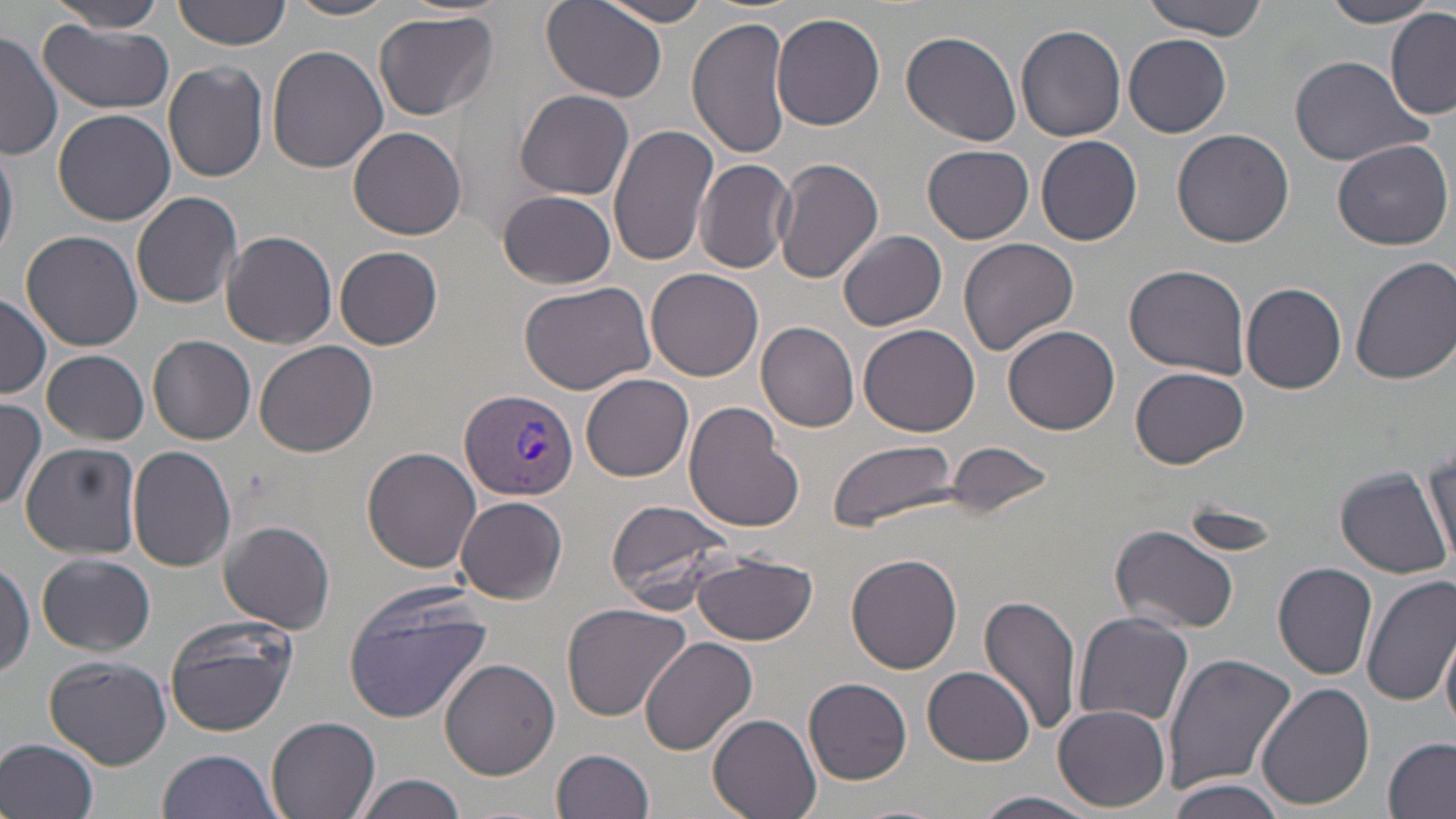 Approximate bounding boxes as [x1, y1, x2, y2] in pixels. Uninfected red blood cell locations: [44, 0, 170, 31], [173, 0, 292, 51], [1140, 0, 1273, 40], [283, 1, 399, 21], [540, 1, 670, 104], [602, 1, 713, 26], [1321, 1, 1439, 27], [373, 10, 499, 121], [1386, 11, 1456, 120], [771, 12, 887, 130], [687, 17, 793, 160], [41, 20, 177, 113], [1016, 25, 1127, 142], [900, 29, 1021, 147], [0, 30, 61, 160], [1124, 33, 1231, 137], [267, 45, 390, 175], [1288, 54, 1431, 166], [163, 61, 269, 182], [517, 89, 633, 200], [52, 108, 176, 226], [608, 123, 719, 269], [348, 125, 466, 239], [1172, 128, 1295, 247], [1036, 135, 1142, 246], [0, 139, 19, 264], [1332, 140, 1453, 251], [923, 145, 1033, 243], [772, 157, 884, 283], [695, 160, 798, 274], [131, 191, 243, 311], [498, 191, 618, 288], [20, 229, 144, 351], [839, 230, 947, 331], [222, 231, 337, 348], [958, 237, 1078, 356], [335, 246, 443, 349], [1350, 255, 1456, 386], [1124, 263, 1251, 379], [646, 267, 763, 383], [517, 279, 658, 396], [1242, 283, 1348, 393], [0, 295, 49, 398], [756, 322, 860, 433], [859, 323, 980, 437], [1003, 325, 1120, 435], [149, 335, 256, 444], [255, 339, 377, 458], [42, 350, 149, 445], [1131, 367, 1249, 467], [581, 373, 693, 482], [0, 399, 47, 511], [683, 402, 805, 534], [828, 438, 958, 530], [21, 442, 141, 558], [942, 442, 1060, 508], [128, 445, 238, 573], [1426, 446, 1455, 564], [364, 447, 482, 573], [1336, 467, 1453, 579], [455, 497, 568, 604], [604, 499, 740, 614], [1179, 502, 1286, 557], [219, 519, 336, 633], [1111, 524, 1241, 636], [692, 551, 819, 646], [38, 553, 155, 655], [846, 554, 963, 675], [0, 557, 34, 680], [1272, 563, 1378, 680], [1362, 574, 1456, 705], [343, 590, 495, 723], [980, 593, 1083, 739], [560, 601, 694, 720], [1073, 612, 1195, 729], [163, 616, 296, 736], [1440, 627, 1456, 739], [640, 635, 758, 755], [1161, 652, 1298, 796], [45, 654, 172, 768], [441, 659, 561, 780], [924, 665, 1035, 764], [805, 677, 913, 785], [1255, 681, 1375, 811], [10, 690, 143, 811], [1054, 704, 1171, 810], [709, 714, 822, 819], [265, 716, 380, 819], [0, 736, 100, 819], [1384, 738, 1455, 817], [555, 749, 656, 819], [154, 751, 283, 819], [358, 773, 467, 819], [1169, 780, 1285, 819], [977, 791, 1101, 819]. Plasmodium vivax-infected red blood cell locations: [461, 388, 578, 501]. Slide-level diagnosis: Plasmodium vivax. May-Grünwald-Giemsa stain. Image is 1456×819 pixels. Thin blood film. Captured at 1000x magnification. One field of a larger specimen. Light microscopy.